Give the position of every leukocyte visible.
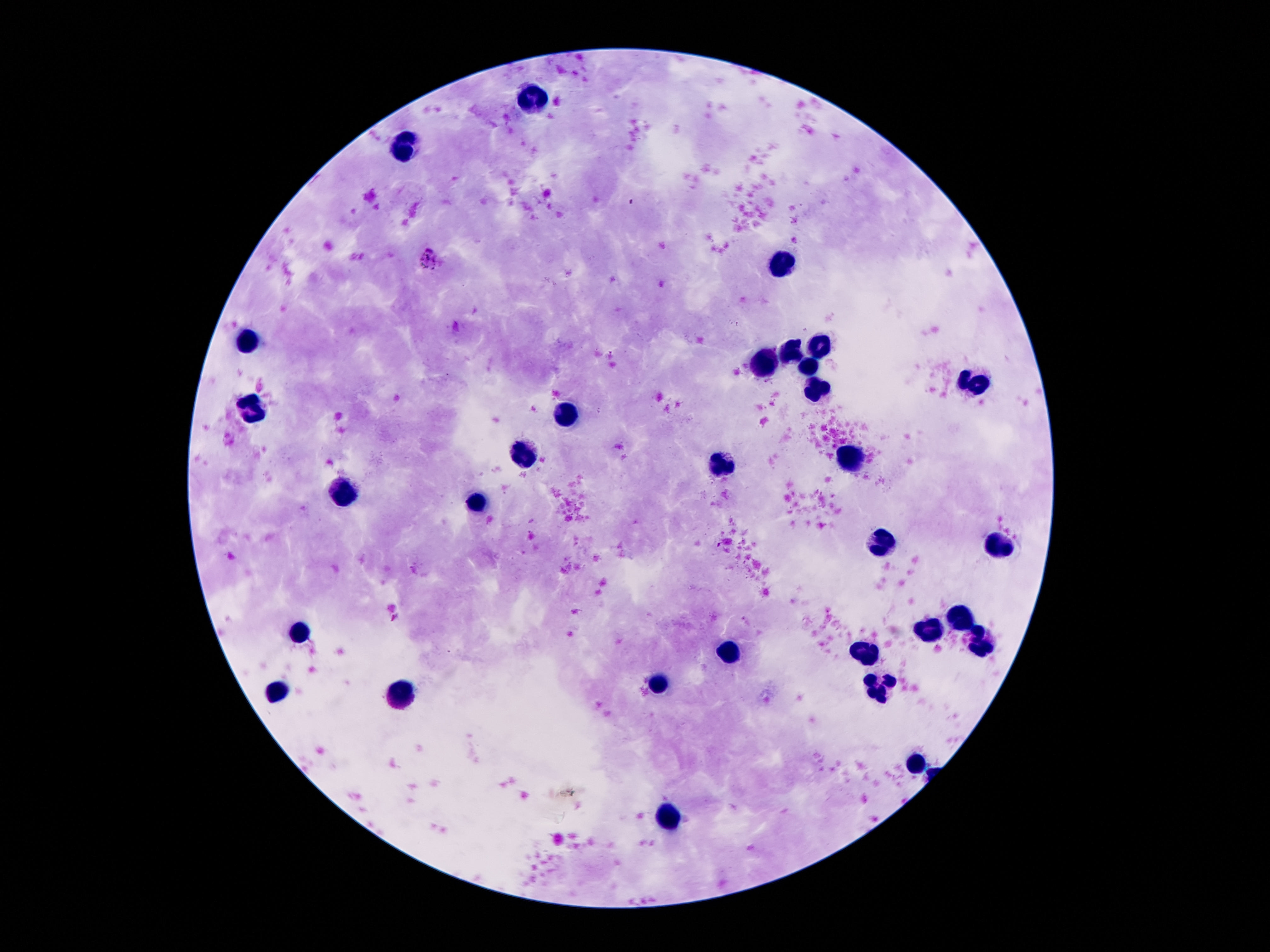

Approximate centers as {x, y} in pixels.
Leukocytes: {535, 98}, {408, 145}, {783, 266}, {250, 342}, {820, 346}, {791, 353}, {766, 361}, {809, 363}, {975, 383}, {817, 389}, {254, 405}, {568, 415}, {527, 452}, {852, 459}, {727, 465}, {344, 495}, {479, 504}, {1000, 545}, {883, 547}, {963, 621}, {303, 633}, {932, 633}, {981, 646}, {871, 649}, {729, 653}, {664, 682}, {881, 683}, {279, 692}, {395, 696}, {912, 762}, {666, 817}.

Image is 1270×952 pixels. Thick blood film. One field from this slide. Giemsa stain. Smartphone photograph taken through the microscope eyepiece. Patient malaria status: uninfected. 100x magnification.